Identify the cell.
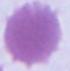
This is an erythrocyte.

Micrograph. Captured at 1000x magnification.